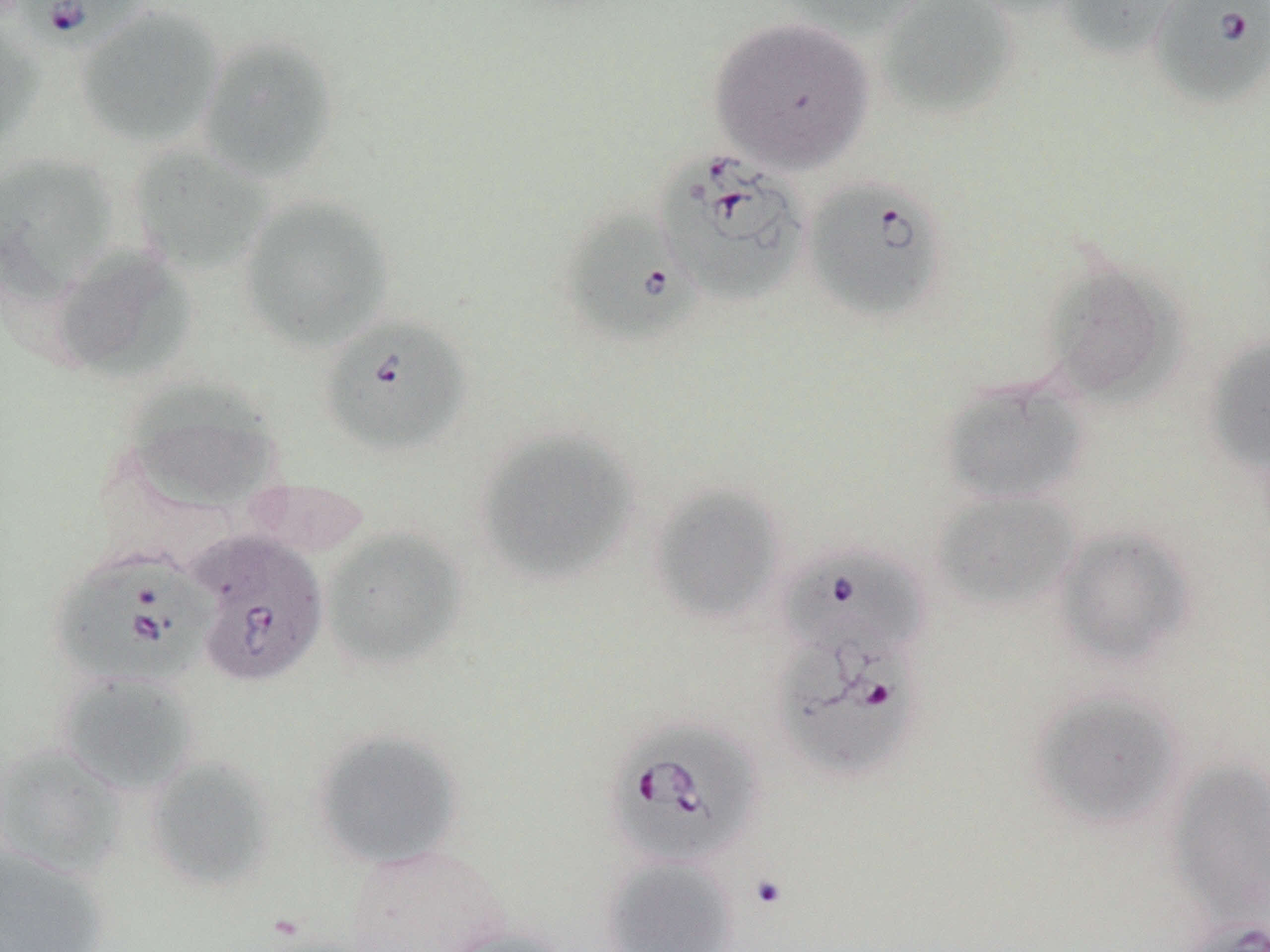
Approximate bounding boxes as [x1, y1, x2, y2] in pixels. Babesia divergens-infected red blood cell locations: [8, 0, 151, 50], [1149, 1, 1270, 107], [653, 150, 807, 306], [800, 177, 949, 323], [561, 206, 698, 348], [317, 314, 472, 459], [191, 531, 326, 687], [779, 547, 928, 662], [50, 550, 213, 688], [772, 629, 925, 781], [603, 719, 764, 870], [1182, 919, 1270, 952]. Uninfected red blood cell locations: [779, 0, 937, 37], [875, 0, 1019, 119], [1057, 0, 1183, 60], [75, 6, 225, 149], [0, 17, 45, 153], [708, 17, 875, 173], [197, 35, 339, 184], [128, 146, 273, 275], [0, 152, 119, 302], [238, 195, 395, 352], [48, 245, 195, 382], [1041, 261, 1183, 406], [1204, 335, 1270, 477], [938, 376, 1090, 506], [124, 380, 283, 510], [474, 429, 641, 585], [240, 478, 371, 560], [648, 485, 786, 624], [930, 490, 1080, 614], [1052, 525, 1196, 667], [321, 526, 467, 671], [56, 671, 200, 796], [1027, 687, 1187, 830], [312, 728, 464, 870], [0, 744, 127, 878], [144, 756, 277, 890], [1168, 757, 1270, 926], [0, 844, 110, 952], [341, 844, 510, 952], [601, 855, 739, 952], [441, 924, 571, 952]. Slide-level diagnosis: Babesia divergens. Single field of view. May-Grünwald-Giemsa-stained preparation. Image is 1270×952 pixels. Captured at 1000x magnification. Optical microscopy. Thin blood smear.